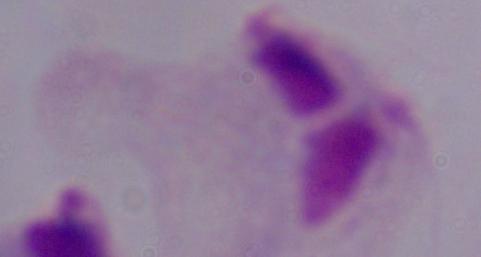
Photomicrograph. 1000x magnification. A trichomonad is shown.